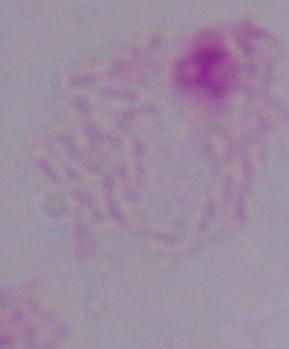
Captured at 1000x magnification. Micrograph. A trichomonad is shown.